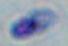

Summary:
  - Modality: micrograph
  - Magnification: 1000x
  - Identification: Toxoplasma gondii